Give the position of every Plasmodium parasite.
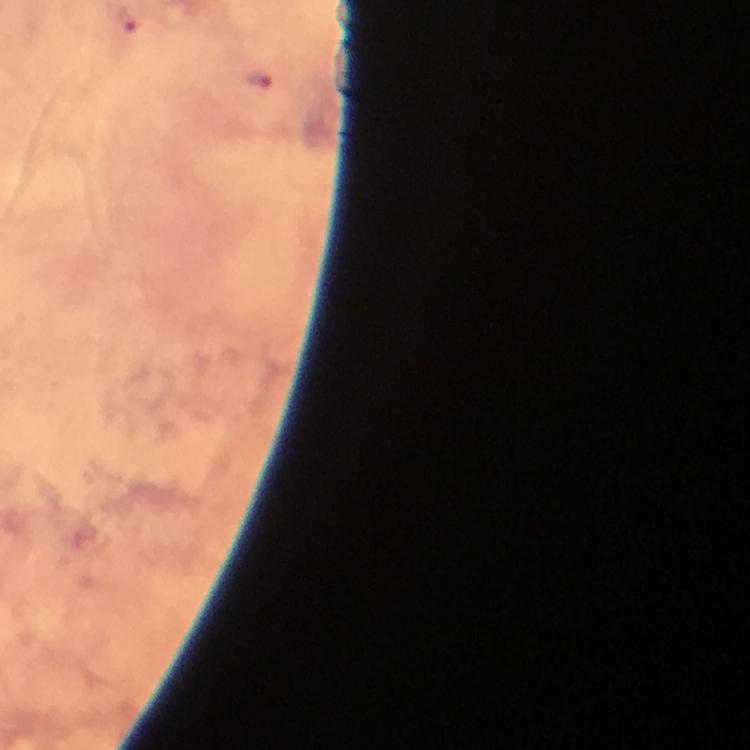
Approximate object centers, in pixels from the top-left corner.
Plasmodium parasites: (x=127, y=23), (x=260, y=81).

Summary:
  - Stain: Giemsa
  - Context: from a malaria diagnostic workup
  - Preparation: thick blood film
  - Image size: 750×750 pixels
  - Cropped from: a single field of view
  - Capture: smartphone camera through the microscope
  - Immersion oil: used
  - Magnification: 100x